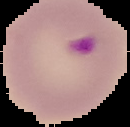
image type = segmented cell region on a black background
result = Plasmodium parasites detected
preparation = thin blood film
image size = 130×127 pixels